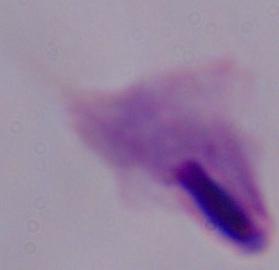
modality = photomicrograph
identification = trichomonad
magnification = 1000x